Name the blood parasite species.
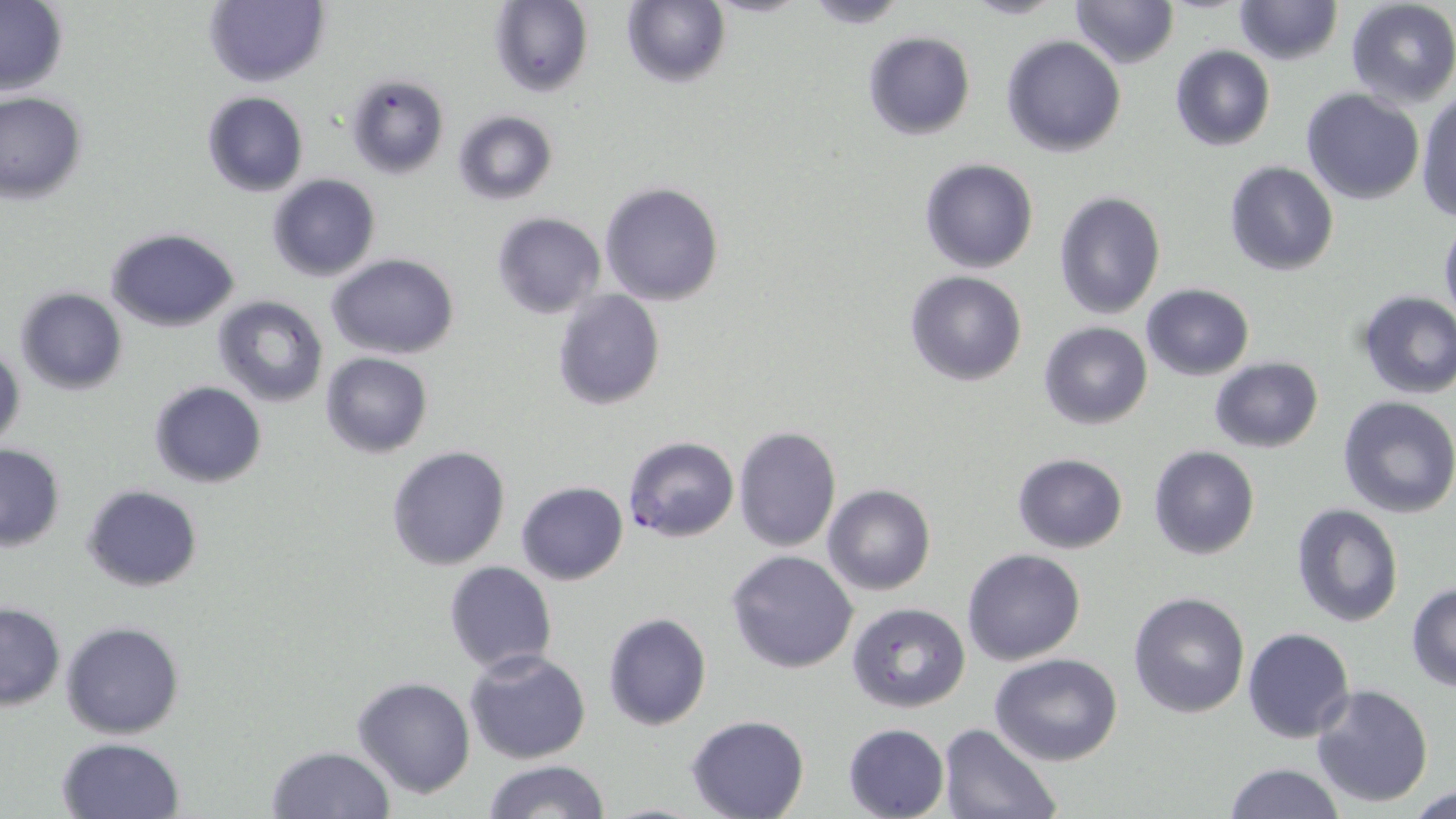

Plasmodium falciparum.

Approximate bounding boxes as (x1,y1)-(x2,y2) corner pairs in pixels. Plasmodium falciparum-infected red blood cell locations: (622,435)-(740,542). Uninfected red blood cell locations: (204,0)-(329,88), (800,0)-(913,27), (957,0)-(1069,20), (1068,0)-(1179,69), (1233,0)-(1343,66), (488,1)-(593,98), (620,1)-(731,88), (1344,1)-(1456,110), (0,3)-(70,95), (862,31)-(976,140), (1001,35)-(1126,156), (1169,44)-(1275,151), (343,72)-(450,180), (1301,89)-(1425,205), (1416,91)-(1456,224), (202,92)-(308,196), (0,93)-(87,203), (451,110)-(558,206), (919,158)-(1037,274), (1224,160)-(1339,276), (266,174)-(380,281), (599,181)-(725,305), (1053,191)-(1166,320), (491,212)-(605,319), (1439,221)-(1456,329), (104,228)-(240,330), (327,254)-(459,359), (904,271)-(1029,387), (1141,284)-(1254,380), (15,288)-(126,395), (552,289)-(665,411), (1356,290)-(1456,400), (212,295)-(330,408), (1039,322)-(1152,430), (1,338)-(24,451), (319,352)-(433,458), (1209,358)-(1323,452), (149,380)-(266,489), (1337,397)-(1456,518), (733,425)-(842,552), (0,444)-(65,551), (386,445)-(511,570), (1149,445)-(1259,561), (1012,453)-(1128,553), (514,481)-(629,585), (82,484)-(202,592), (823,485)-(935,596), (1291,503)-(1402,628), (962,548)-(1085,666), (726,550)-(859,675), (444,560)-(557,675), (1406,582)-(1456,691), (1128,591)-(1250,718), (0,601)-(64,710), (847,603)-(970,714), (603,612)-(713,731), (61,621)-(185,738), (1243,627)-(1355,744), (464,649)-(590,764), (990,653)-(1123,767), (351,675)-(477,799), (1311,684)-(1433,807), (686,715)-(811,819), (843,722)-(948,818), (937,724)-(1060,818), (56,737)-(185,819), (265,745)-(396,819), (482,761)-(612,818), (1223,762)-(1345,819), (1408,786)-(1456,819). May-Grünwald-Giemsa-stained preparation. Image is 1456×819 pixels. 1000x magnification. Single field of view. Light microscopy. Thin blood smear.